Locate the cells, classifying each as a parasitized red blood cell, an uninfected red blood cell, or a white blood cell.
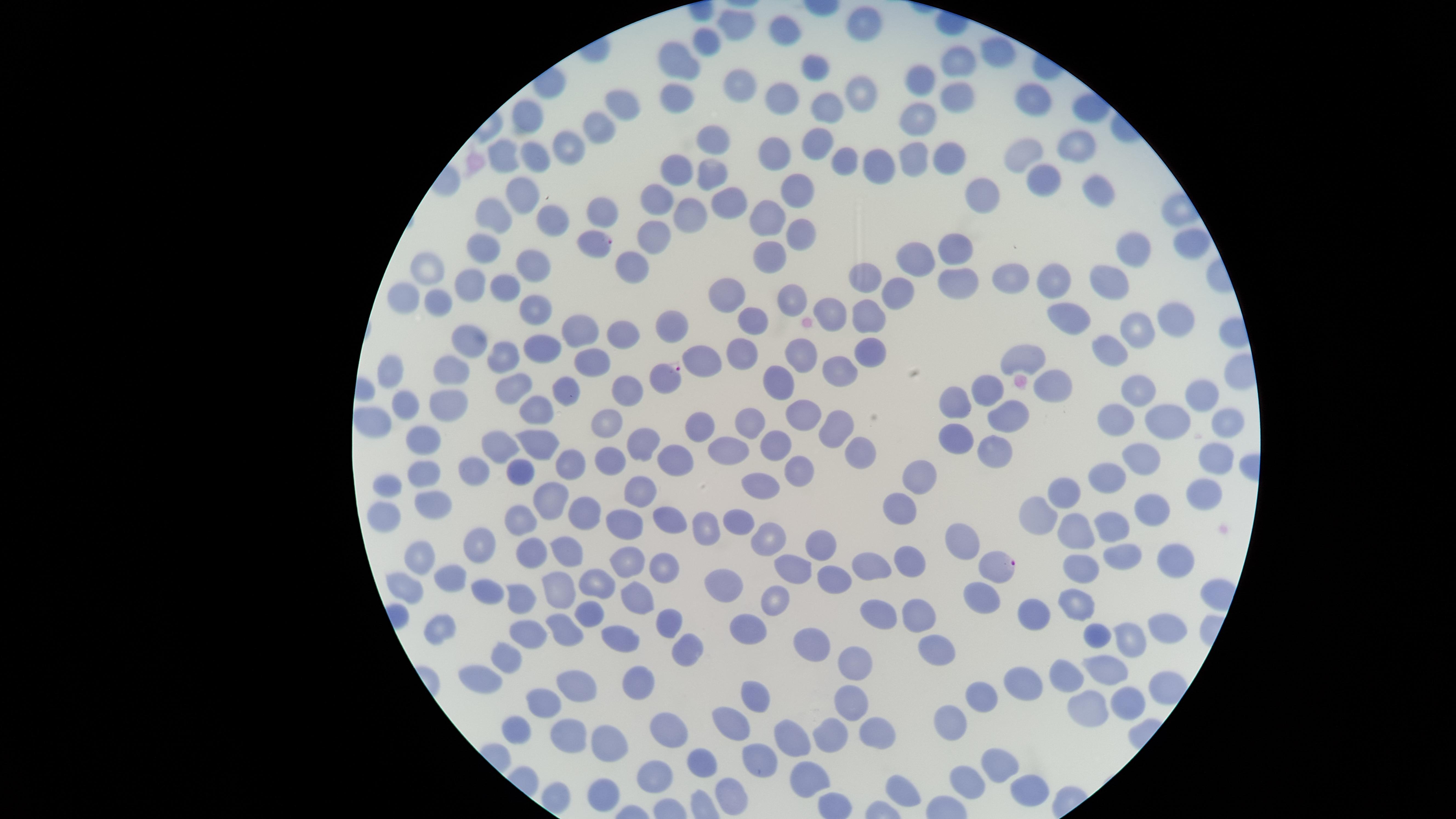
Approximate marker points, in pixels from the top-left corner.
Parasitized red blood cells: (x=596, y=244), (x=667, y=377), (x=1000, y=563).
Uninfected red blood cells: (x=863, y=23), (x=734, y=26), (x=784, y=31), (x=710, y=41), (x=1000, y=53), (x=680, y=60), (x=952, y=66), (x=816, y=68), (x=731, y=81), (x=917, y=81), (x=790, y=94), (x=859, y=96), (x=953, y=96), (x=620, y=102), (x=675, y=102), (x=1033, y=103), (x=829, y=111), (x=529, y=118), (x=920, y=118), (x=592, y=127), (x=708, y=136), (x=815, y=140), (x=1072, y=142), (x=779, y=146), (x=567, y=147), (x=505, y=150), (x=1033, y=154), (x=533, y=155), (x=955, y=155), (x=917, y=156), (x=837, y=163), (x=868, y=166), (x=678, y=168), (x=706, y=174), (x=1040, y=180), (x=1094, y=185), (x=795, y=186), (x=976, y=189), (x=517, y=192), (x=660, y=197), (x=723, y=203), (x=608, y=211), (x=493, y=212), (x=687, y=216), (x=549, y=220), (x=769, y=222), (x=654, y=235), (x=794, y=235), (x=1187, y=240), (x=488, y=244), (x=953, y=247), (x=1133, y=248), (x=769, y=258), (x=921, y=260), (x=429, y=266), (x=532, y=267), (x=629, y=273), (x=1007, y=277), (x=1059, y=277), (x=866, y=278), (x=1111, y=278), (x=953, y=281), (x=467, y=283), (x=504, y=286), (x=899, y=291), (x=729, y=294), (x=794, y=294), (x=405, y=295), (x=436, y=299), (x=531, y=304), (x=833, y=308), (x=1065, y=316), (x=870, y=319), (x=749, y=322), (x=1173, y=324), (x=577, y=325), (x=674, y=330), (x=1138, y=330), (x=614, y=332), (x=470, y=340), (x=540, y=344), (x=866, y=349), (x=1116, y=349), (x=736, y=351), (x=512, y=353), (x=794, y=355), (x=1029, y=358), (x=593, y=360), (x=700, y=366), (x=454, y=368), (x=837, y=370), (x=395, y=371), (x=513, y=385), (x=564, y=385), (x=626, y=385), (x=1057, y=385), (x=989, y=387), (x=1137, y=388), (x=779, y=390), (x=1202, y=395), (x=957, y=400), (x=406, y=401), (x=441, y=403), (x=535, y=403), (x=1003, y=413), (x=799, y=415), (x=1117, y=416), (x=602, y=418), (x=376, y=420), (x=1161, y=420), (x=1225, y=421), (x=748, y=425), (x=832, y=425), (x=693, y=429), (x=956, y=431), (x=642, y=441), (x=779, y=441), (x=421, y=443), (x=503, y=443), (x=539, y=443), (x=989, y=443), (x=731, y=450), (x=860, y=450), (x=1143, y=454), (x=620, y=455), (x=1214, y=457), (x=671, y=459), (x=565, y=468), (x=468, y=470), (x=519, y=472), (x=797, y=472), (x=421, y=474), (x=1111, y=475), (x=920, y=476), (x=761, y=484), (x=1070, y=486), (x=642, y=487), (x=386, y=488), (x=1203, y=492), (x=547, y=493), (x=430, y=503), (x=1155, y=509), (x=582, y=511), (x=895, y=515), (x=1041, y=515), (x=667, y=517), (x=383, y=519), (x=520, y=522), (x=738, y=522), (x=626, y=524), (x=1116, y=526), (x=704, y=530), (x=1069, y=535), (x=964, y=536), (x=768, y=540), (x=825, y=544), (x=481, y=548), (x=569, y=548), (x=532, y=552), (x=1121, y=552), (x=421, y=559), (x=870, y=559), (x=631, y=562), (x=910, y=562), (x=1082, y=562), (x=1170, y=562), (x=663, y=565), (x=794, y=566), (x=594, y=581), (x=830, y=581), (x=450, y=584), (x=725, y=585), (x=562, y=586), (x=404, y=588), (x=492, y=588), (x=982, y=594), (x=523, y=599), (x=633, y=599), (x=775, y=602), (x=1081, y=606), (x=914, y=609), (x=1040, y=609), (x=591, y=610), (x=880, y=610), (x=670, y=620), (x=745, y=625), (x=439, y=627), (x=1159, y=629), (x=530, y=630), (x=563, y=630), (x=622, y=631), (x=1099, y=631), (x=1132, y=637), (x=811, y=640), (x=930, y=644), (x=683, y=648), (x=510, y=653), (x=852, y=658), (x=1105, y=662), (x=1065, y=671), (x=483, y=679), (x=636, y=682), (x=1027, y=682), (x=578, y=684), (x=985, y=691), (x=756, y=694), (x=1081, y=700), (x=543, y=703), (x=1126, y=703), (x=848, y=705), (x=736, y=719), (x=955, y=723), (x=832, y=725), (x=670, y=727), (x=880, y=727), (x=520, y=729), (x=570, y=731), (x=796, y=736), (x=608, y=741), (x=1000, y=761), (x=708, y=765), (x=766, y=765), (x=654, y=777), (x=812, y=780), (x=967, y=781), (x=902, y=787), (x=1029, y=787), (x=604, y=793), (x=736, y=804).
No white blood cells identified.

field of view = single
image size = 1456×819 pixels
stain = Giemsa
preparation = thin blood smear
species = Plasmodium falciparum
visible region = circular
capture = smartphone photograph through the microscope eyepiece